Report the malaria status of this cell.
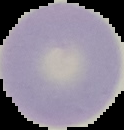
It is uninfected.

Summary:
  - Preparation: thin blood smear
  - Image size: 124×130 pixels
  - Image type: cell region segmented out of the field of view; surrounding area masked to black